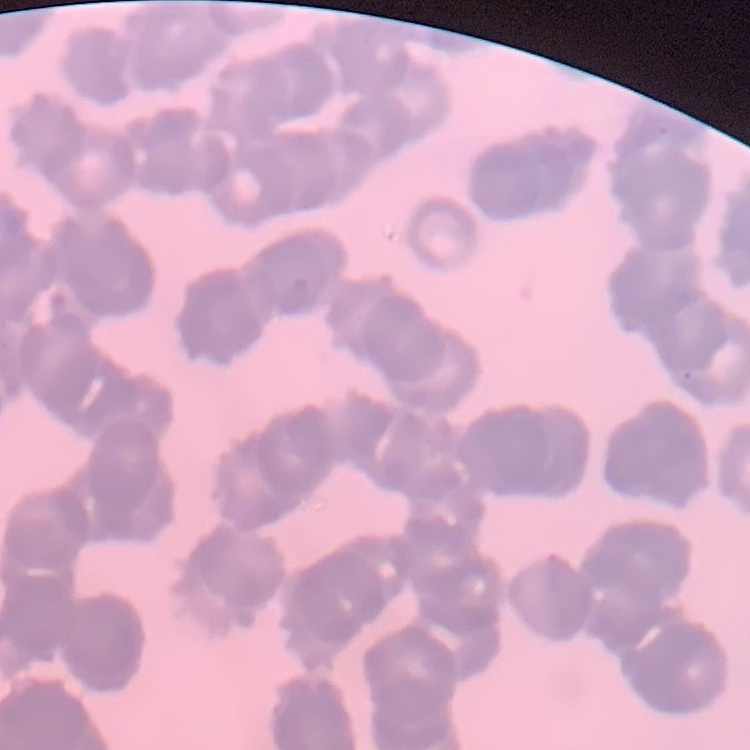

The erythrocytes show rouleaux formation. Field's or Giemsa stain. Thin blood film. Square crop of a larger photomicrograph.